Report the malaria status of this cell.
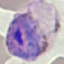

It is parasitized.

{
  "stain": "Giemsa",
  "capture": "smartphone camera at the microscope eyepiece",
  "image_type": "cell patch, automatically extracted from a larger field of view and resized to 64 × 64 pixels",
  "preparation": "thin blood film"
}